Comment on the morphology of the red blood cells.
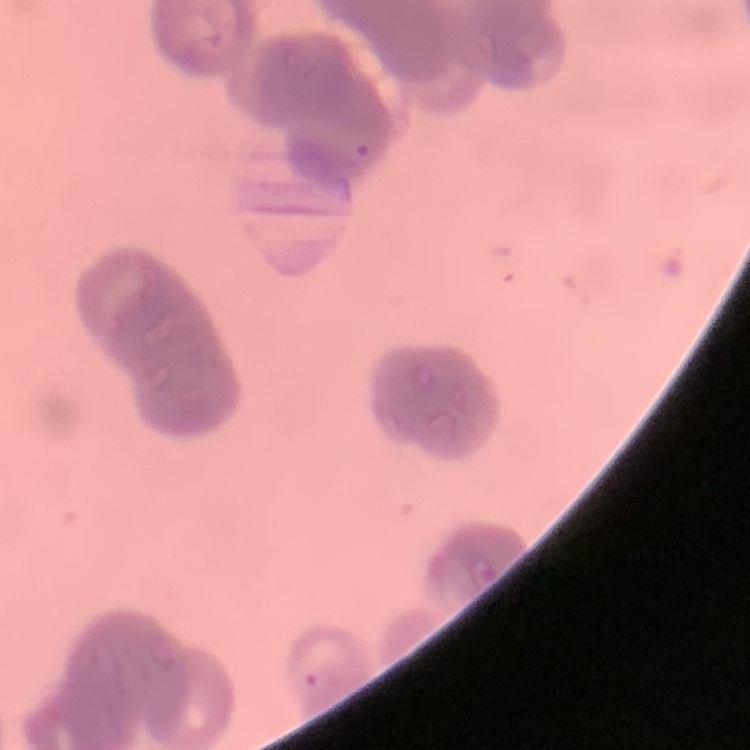
They show rouleaux formation.

Summary:
  - Stain: Field's or Giemsa
  - Image type: one tile cut from a larger photomicrograph
  - Preparation: thin peripheral smear